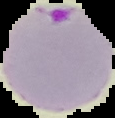

malaria status = parasitized
image type = segmented cell region on a black background
image size = 115×118 pixels
preparation = thin blood film